Assess the morphology of the red blood cells.
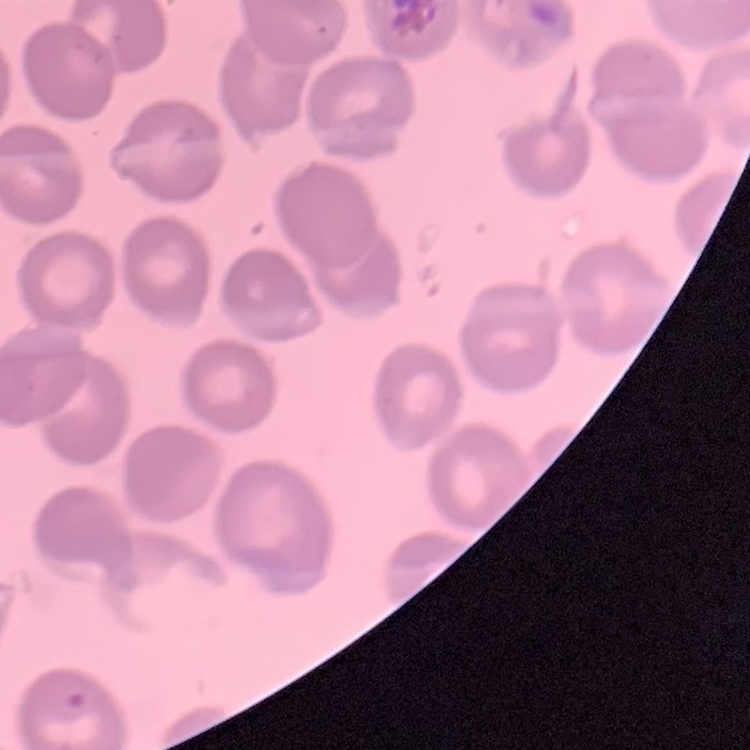

They show no rouleaux formation.

Square crop of a larger photomicrograph. Field's or Giemsa stain. Thin blood film.